Report the malaria status of this cell.
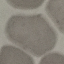

It is uninfected.

Summary:
  - Capture: smartphone camera at the microscope eyepiece
  - Image type: cell patch, automatically extracted from a larger field of view and resized to 64 × 64 pixels
  - Preparation: thin smear
  - Stain: Giemsa